Outline each blood parasite and name the species.
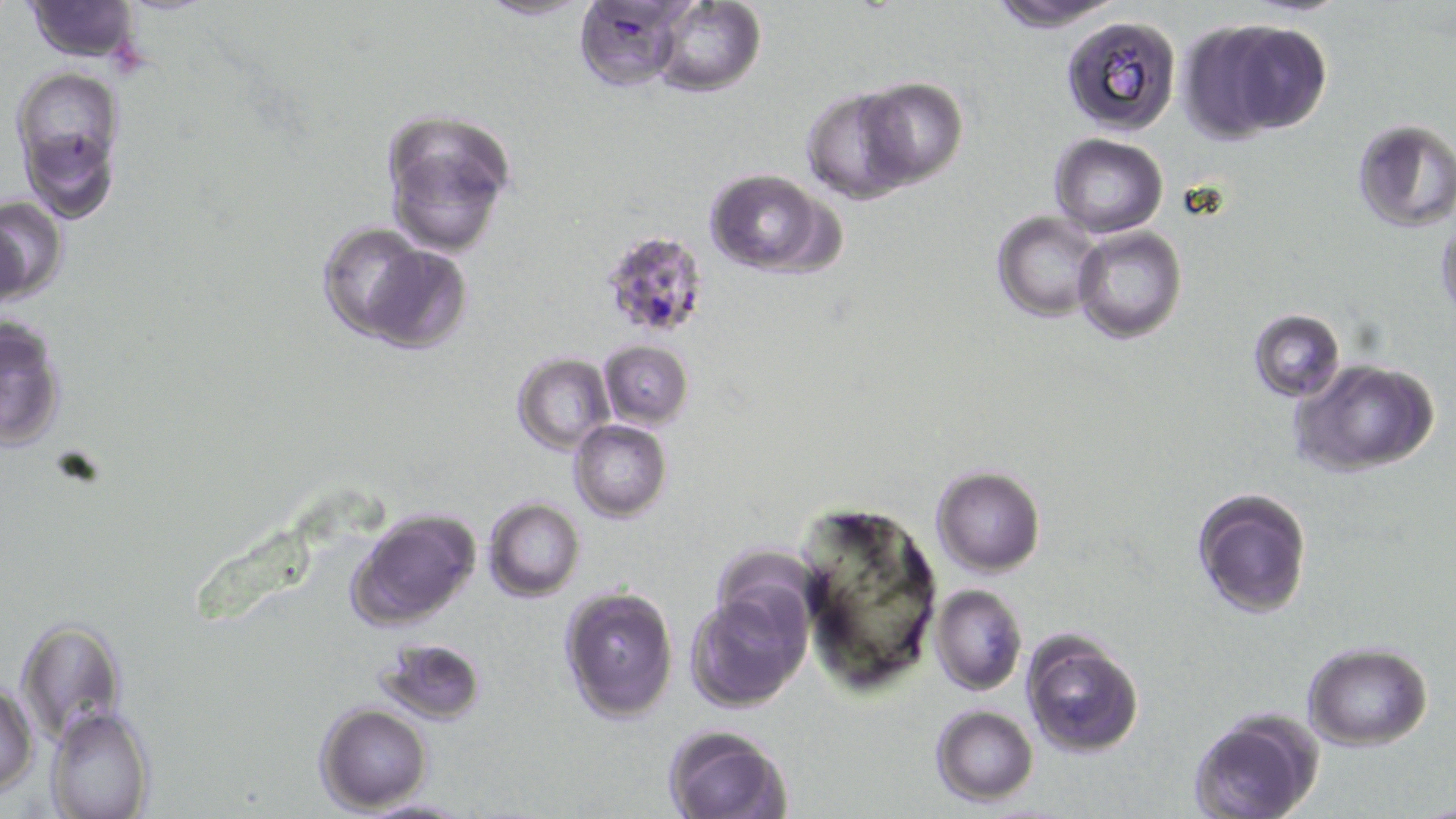
Approximate bounding boxes as (x1, y1, x2, y2) in pixels.
Plasmodium falciparum-infected red blood cells: (599, 230, 711, 342).
No Plasmodium ovale, Plasmodium malariae, Plasmodium vivax, Babesia divergens, or Trypanosoma brucei observed.

{
  "slide_level_diagnosis": "Plasmodium falciparum",
  "preparation": "thin blood smear",
  "modality": "light microscopy",
  "image_size": "1456×819 pixels",
  "field_of_view": "single",
  "uninfected_red_blood_cell_locations": "approximate bounding boxes as (x1, y1, x2, y2) in pixels: (475, 0, 595, 21), (576, 0, 693, 91), (986, 0, 1123, 32), (24, 1, 142, 62), (649, 1, 764, 97), (1060, 12, 1183, 138), (1197, 15, 1333, 137), (14, 67, 124, 179), (853, 76, 970, 189), (798, 86, 921, 203), (380, 107, 515, 256), (1350, 119, 1456, 233), (18, 124, 119, 224), (1049, 134, 1169, 237), (701, 169, 837, 277), (0, 195, 67, 304), (992, 211, 1103, 322), (1435, 211, 1455, 321), (318, 226, 462, 350), (1071, 227, 1187, 344), (1247, 308, 1345, 402), (1, 313, 68, 453), (597, 339, 693, 429), (513, 354, 614, 454), (1292, 358, 1441, 476), (571, 420, 671, 521), (932, 466, 1045, 575), (1191, 488, 1313, 617), (484, 498, 586, 602), (794, 502, 941, 693), (347, 507, 479, 628), (931, 584, 1027, 695), (560, 585, 678, 723), (687, 588, 807, 710), (14, 617, 127, 745), (1020, 629, 1147, 757), (375, 636, 486, 725), (1303, 642, 1433, 750), (1, 674, 39, 797), (316, 703, 433, 812), (930, 705, 1039, 805), (46, 707, 156, 819), (1188, 710, 1322, 819), (662, 724, 791, 819), (354, 797, 470, 817)",
  "magnification": "1000x",
  "stain": "May-Grünwald-Giemsa"
}